State which cell type is depicted.
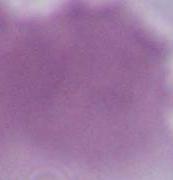
An erythrocyte.

Summary:
  - Magnification: 1000x
  - Modality: photomicrograph